Classify this cell by malaria status.
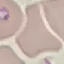

Parasitized.

Thin smear of blood. Photographed with a smartphone camera at the microscope eyepiece. Giemsa-stained preparation. Cell patch, automatically extracted from a larger field of view and resized to 64 × 64 pixels.